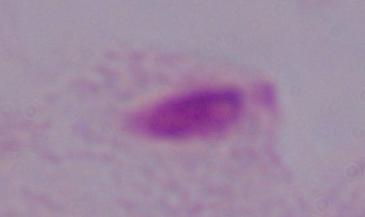

1000x magnification. Micrograph. A trichomonad is shown.